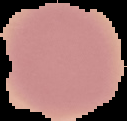
preparation = thin blood smear
malaria status = uninfected
image size = 127×121 pixels
image type = segmented cell region on a black background